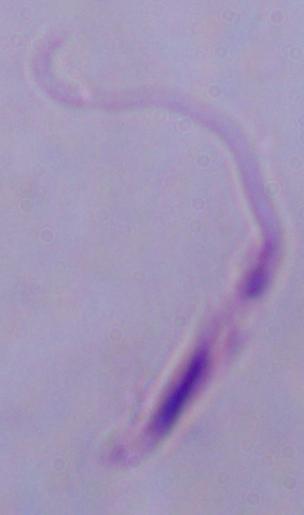

{
  "identification": "Leishmania",
  "magnification": "1000x",
  "modality": "photomicrograph"
}